Name the cell type shown.
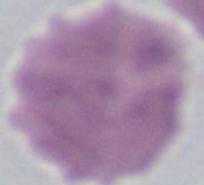
An erythrocyte.

Summary:
  - Modality: photomicrograph
  - Magnification: 1000x